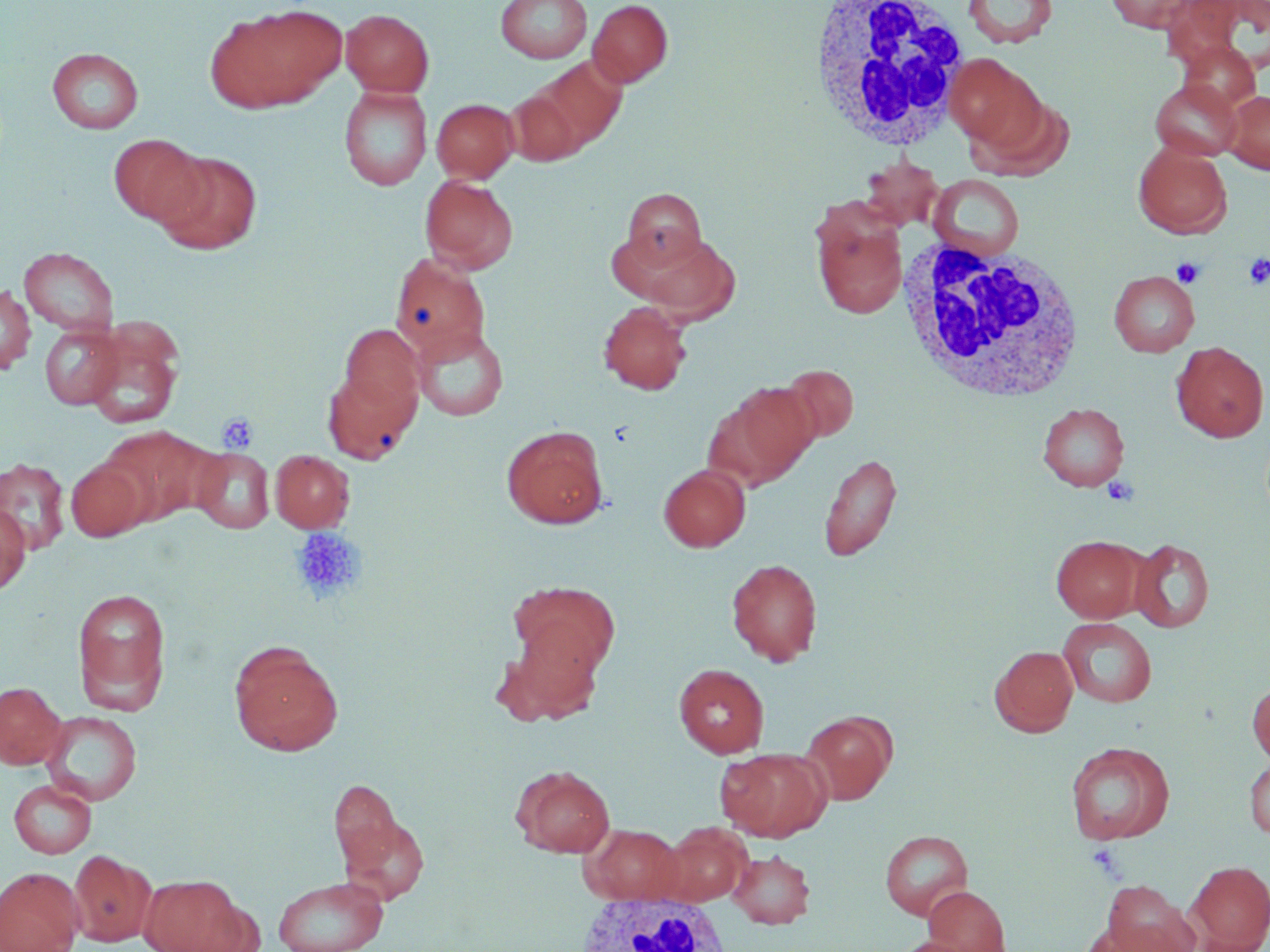

{
  "slide_level_diagnosis": "negative for blood parasites",
  "white_blood_cell_locations": "approximate bounding boxes as (x1, y1, x2, y2) in pixels: (806, 2, 973, 152), (892, 241, 1091, 401), (572, 892, 734, 951)",
  "platelet_locations": "approximate bounding boxes as (x1, y1, x2, y2) in pixels: (1243, 253, 1270, 290), (1173, 258, 1205, 288), (216, 412, 257, 452), (290, 527, 365, 604), (1087, 844, 1126, 880)",
  "stain": "May-Grünwald-Giemsa",
  "uninfected_red_blood_cell_locations": "approximate bounding boxes as (x1, y1, x2, y2) in pixels: (496, 0, 592, 63), (587, 0, 674, 88), (963, 0, 1058, 48), (1103, 0, 1202, 32), (236, 4, 349, 104), (340, 8, 434, 97), (202, 14, 306, 113), (1175, 39, 1262, 116), (47, 47, 144, 134), (945, 54, 1045, 151), (530, 55, 628, 155), (1150, 78, 1244, 161), (338, 86, 433, 191), (506, 87, 584, 166), (1221, 90, 1270, 174), (969, 93, 1075, 180), (431, 98, 519, 183), (107, 133, 208, 227), (1133, 143, 1232, 239), (154, 151, 263, 255), (860, 157, 944, 232), (928, 174, 1025, 259), (420, 175, 518, 273), (622, 188, 706, 268), (813, 214, 907, 319), (628, 229, 741, 324), (18, 246, 120, 336), (389, 253, 492, 369), (1108, 270, 1199, 357), (0, 285, 37, 374), (598, 300, 692, 395), (39, 324, 123, 409), (412, 324, 509, 421), (340, 325, 426, 414), (85, 328, 184, 430), (1170, 341, 1268, 442), (322, 364, 421, 464), (780, 364, 859, 444), (714, 381, 821, 486), (1037, 402, 1130, 491), (97, 425, 210, 526), (501, 425, 608, 529), (191, 447, 274, 534), (270, 450, 354, 533), (818, 451, 902, 562), (0, 457, 71, 555), (66, 458, 149, 542), (658, 463, 750, 552), (0, 503, 31, 595), (1051, 535, 1146, 622), (1129, 538, 1214, 633), (726, 558, 823, 666), (508, 581, 620, 680), (72, 587, 171, 710), (1057, 617, 1158, 708), (494, 622, 607, 725), (228, 640, 344, 756), (990, 645, 1079, 737), (673, 663, 770, 758), (0, 681, 67, 769), (1247, 681, 1270, 765), (41, 710, 143, 806), (800, 711, 896, 804), (1065, 740, 1176, 845), (717, 746, 832, 841), (1244, 757, 1270, 839), (512, 765, 616, 857), (328, 778, 406, 880), (9, 779, 96, 858), (337, 805, 429, 905), (581, 823, 686, 904), (657, 823, 751, 906), (879, 830, 974, 920), (728, 849, 815, 928), (69, 850, 155, 947), (1187, 860, 1270, 951), (0, 867, 84, 952), (138, 874, 248, 951), (273, 875, 389, 952), (1100, 879, 1199, 952), (923, 885, 1012, 951), (1084, 920, 1183, 952), (890, 937, 980, 952)",
  "image_size": "1270×952 pixels",
  "preparation": "thin blood smear",
  "field_of_view": "one of a larger specimen",
  "magnification": "1000x",
  "modality": "optical microscopy"
}